Identify the parasite.
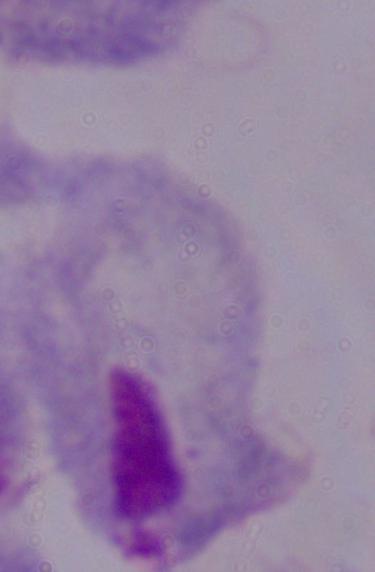

A trichomonad.

magnification = 1000x
modality = photomicrograph